Name the cell type shown.
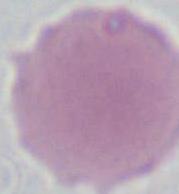
This is an erythrocyte.

{
  "magnification": "1000x",
  "modality": "photomicrograph"
}